Give the position of each Plasmodium falciparum parasite with its life-cycle stage, each leukocyte, and any debris.
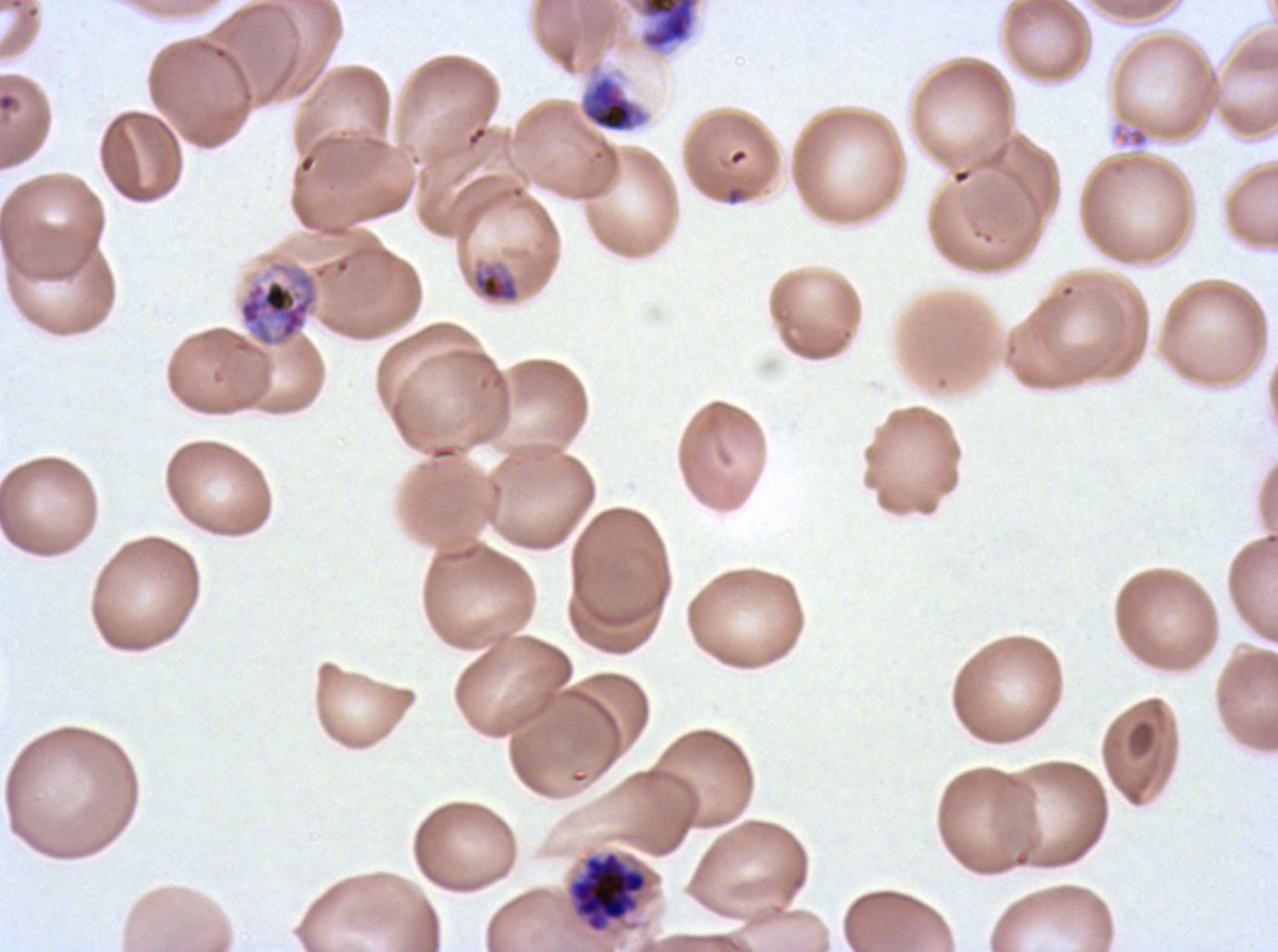

Approximate bounding boxes as (x1, y1, x2, y2) in pixels.
Late-ring/early-trophozoite forms: (473, 269, 520, 302).
Early schizonts: (578, 72, 650, 134), (238, 260, 319, 348).
Late schizonts: (569, 850, 648, 933).
Gametocytes: (627, 0, 702, 55).
Debris: (1111, 121, 1149, 150).
No rings, mid trophozoites, late trophozoites, segmenters, or leukocytes observed.

Summary:
  - Image size: 1278×952 pixels
  - Life-cycle stages observed: late-ring/early-trophozoite, early schizont, late schizont, gametocyte
  - Preparation: thin blood film
  - Field of view: sub-image separated from a larger composite
  - Specimen: Plasmodium falciparum cultured ex vivo for 24 to 48 hours, from a patient in The Gambia
  - Stain: Giemsa